Identify the preparation type.
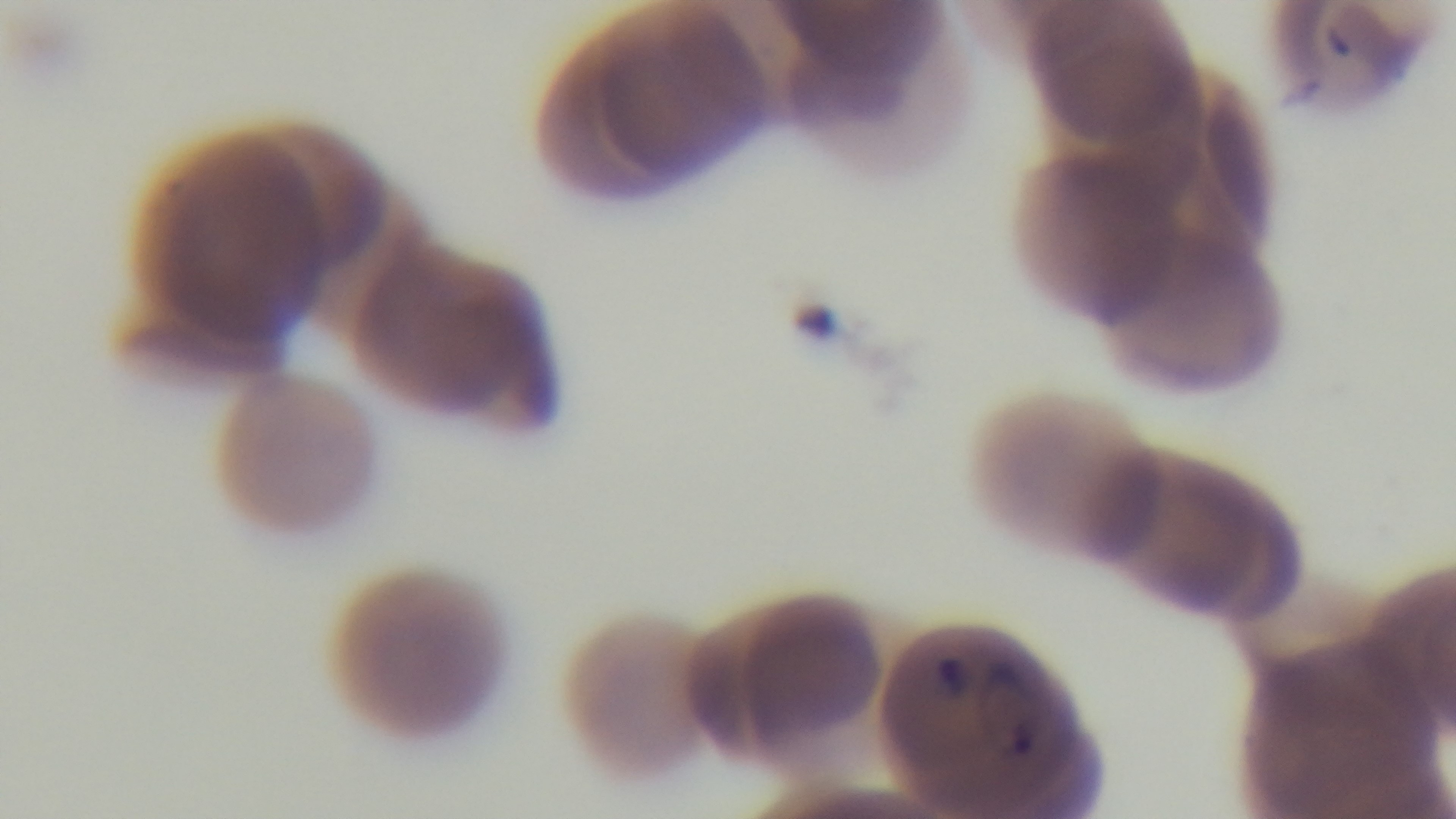
It is a thin blood film.

objective: 100x oil immersion
capture: mounted 4K digital camera
modality: light microscopy
malaria_status: infected
stain: Giemsa
field_of_view: one from the slide